Assess this cell for malaria.
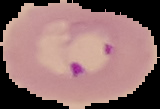
Parasitized.

image size = 160×109 pixels
preparation = thin blood film
image type = segmented cell region with the area outside set to black